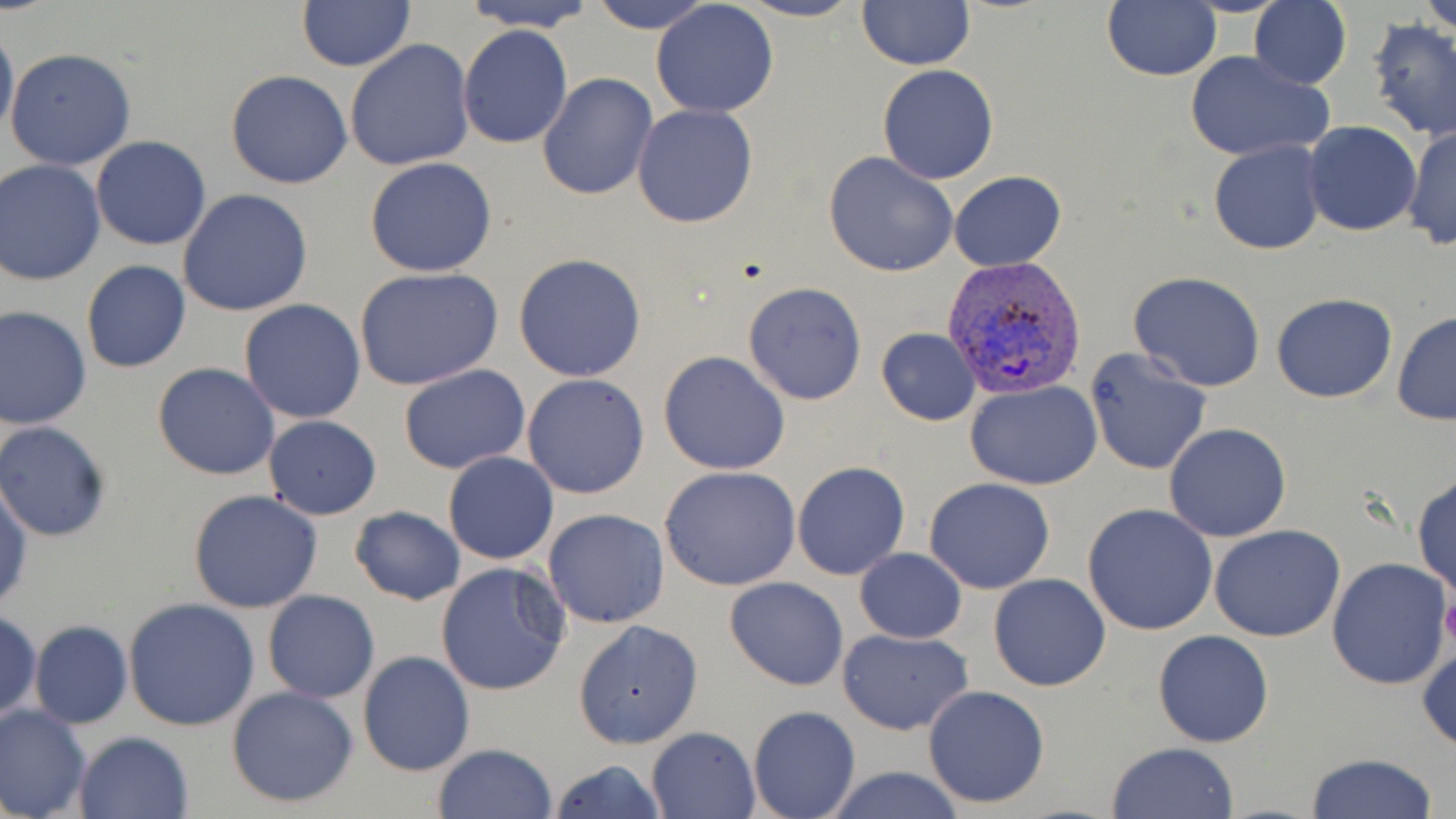
{
  "slide_level_diagnosis": "Plasmodium vivax",
  "stain": "May-Grünwald-Giemsa",
  "field_of_view": "single",
  "uninfected_red_blood_cell_locations": "approximate bounding boxes as (x1,y1)-(x2,y2) corner pairs in pixels: (588,0)-(717,35), (737,0)-(863,22), (1249,0)-(1352,90), (1421,0)-(1456,35), (460,1)-(599,32), (858,1)-(974,70), (1101,1)-(1220,83), (297,2)-(414,71), (650,2)-(779,118), (1366,19)-(1456,141), (1,22)-(18,141), (458,26)-(573,149), (345,40)-(475,173), (5,47)-(135,171), (1183,50)-(1334,162), (879,65)-(999,183), (224,71)-(353,189), (539,74)-(658,200), (632,103)-(759,228), (1302,122)-(1421,236), (1402,123)-(1455,251), (91,136)-(211,252), (1209,140)-(1328,256), (824,151)-(959,278), (364,157)-(498,277), (0,160)-(105,286), (950,171)-(1066,271), (178,188)-(314,317), (513,252)-(646,380), (80,260)-(191,373), (354,268)-(504,392), (1127,272)-(1267,393), (742,281)-(868,405), (1271,291)-(1397,404), (239,298)-(367,424), (0,305)-(92,430), (1391,311)-(1456,426), (876,327)-(981,425), (1084,348)-(1213,475), (659,350)-(791,476), (151,363)-(281,481), (398,364)-(531,474), (522,373)-(652,499), (966,382)-(1101,491), (261,415)-(382,521), (0,422)-(111,541), (1163,422)-(1291,542), (443,451)-(559,565), (792,461)-(910,580), (660,466)-(803,590), (1412,473)-(1455,598), (0,474)-(32,615), (923,477)-(1056,593), (188,489)-(324,612), (1083,503)-(1219,635), (350,505)-(466,605), (542,509)-(671,629), (1209,525)-(1347,643), (853,548)-(966,644), (1326,556)-(1452,691), (435,561)-(571,698), (988,573)-(1111,692), (723,576)-(849,690), (262,590)-(380,704), (121,599)-(262,732), (0,611)-(41,724), (574,619)-(701,749), (29,620)-(132,729), (836,628)-(974,736), (1153,630)-(1274,747), (1417,639)-(1455,753), (357,650)-(475,777), (226,684)-(361,809), (921,684)-(1051,809), (0,704)-(92,818), (748,706)-(861,819), (646,725)-(762,818), (75,731)-(193,819), (1107,742)-(1240,819), (431,743)-(558,819), (1303,753)-(1443,819), (548,758)-(665,818), (819,765)-(968,819)",
  "modality": "light microscopy",
  "platelet_locations": "approximate bounding boxes as (x1,y1)-(x2,y2) corner pairs in pixels: (1440,589)-(1456,653)",
  "plasmodium_vivax_infected_red_blood_cell_locations": "approximate bounding boxes as (x1,y1)-(x2,y2) corner pairs in pixels: (940,255)-(1087,401)",
  "image_size": "1456×819 pixels",
  "preparation": "thin blood smear",
  "magnification": "1000x"
}